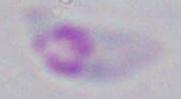
Photomicrograph. 1000x magnification. Toxoplasma gondii is shown.